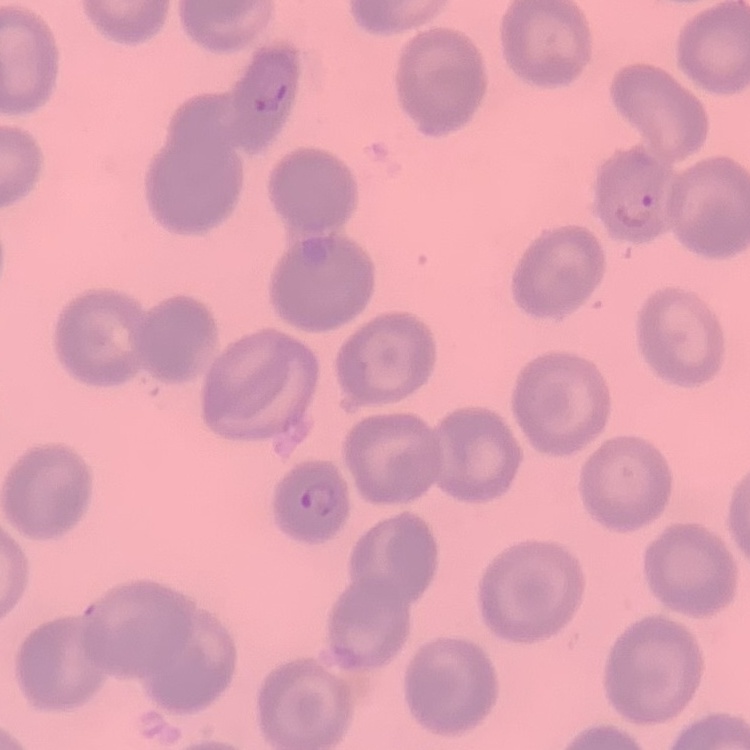
Summary:
  - Erythrocyte morphology: no rouleaux formation
  - Preparation: thin peripheral smear
  - Stain: Field's or Giemsa
  - Image type: one tile cut from a larger photomicrograph